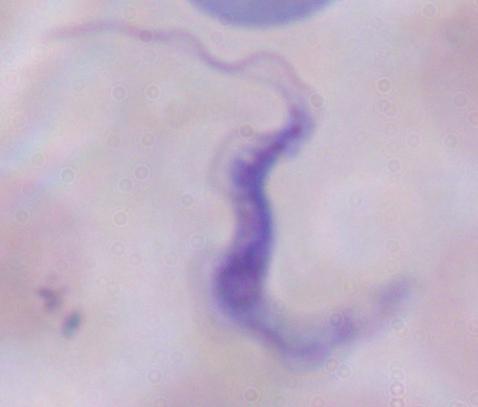

A trypanosome is seen. Captured at 1000x magnification. Photomicrograph.